Give the position of every leukocyte.
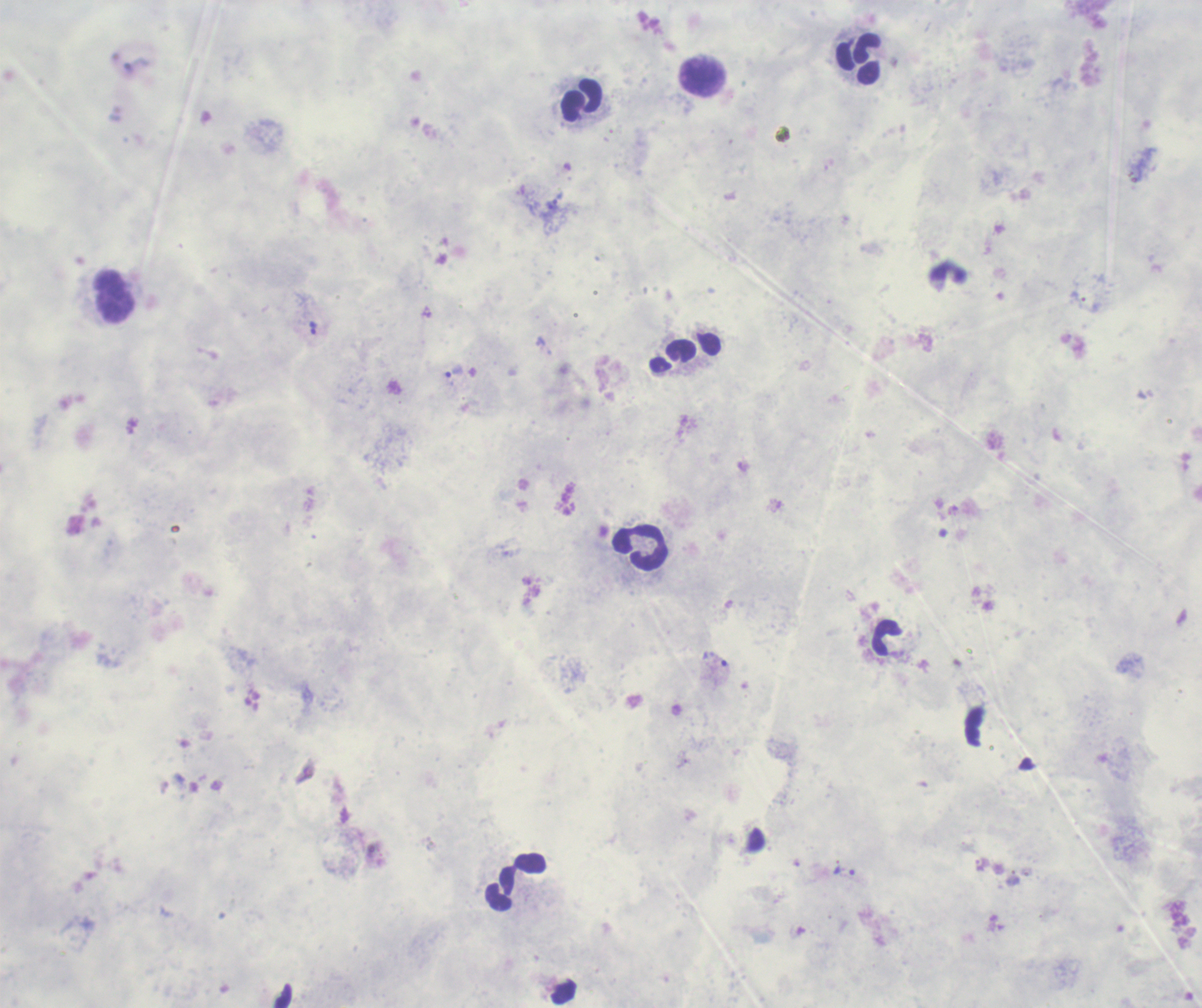
Approximate centers as {x, y} in pixels.
Leukocytes: {859, 59}, {701, 77}, {580, 101}, {115, 297}, {640, 548}, {887, 638}, {516, 882}.

Approximate centers as {x, y} in pixels.
Summary:
  - Trophozoite locations: {313, 328}, {454, 372}, {715, 659}, {844, 871}
  - Stain: Romanowsky
  - Context: previously used in a real diagnosis
  - Field of view: one from this slide
  - Magnification: 100x
  - Result: malaria parasites identified
  - Background quality: unsatisfactory
  - Preparation: thick blood smear
  - Image size: 1202×1008 pixels